Assess the morphology of the erythrocytes.
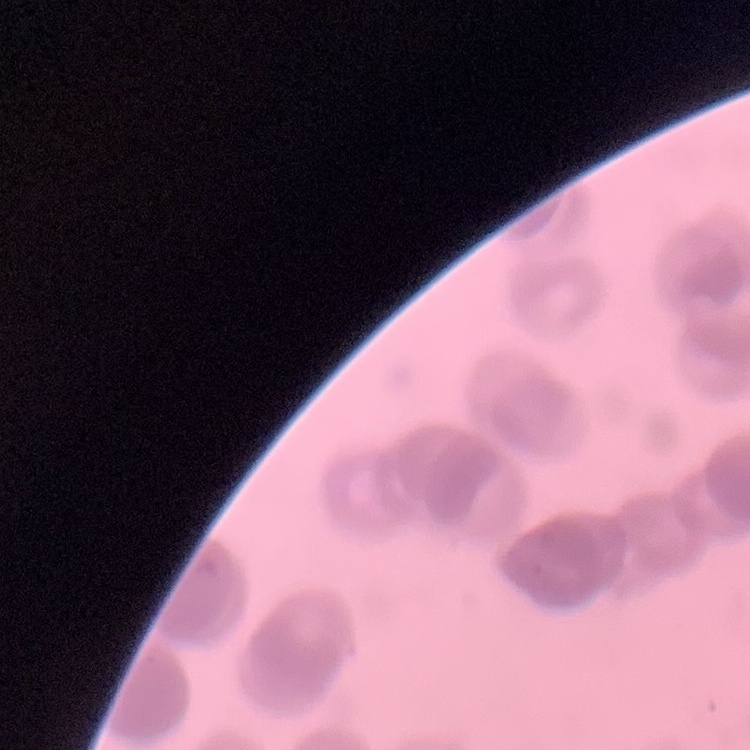

Rouleaux formation.

Stained with either Field's or Giemsa. Square crop of a larger photomicrograph. Thin blood smear.